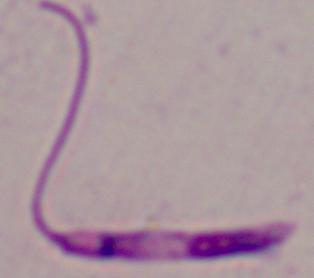
modality = micrograph
magnification = 1000x
identification = Leishmania